Locate platelets.
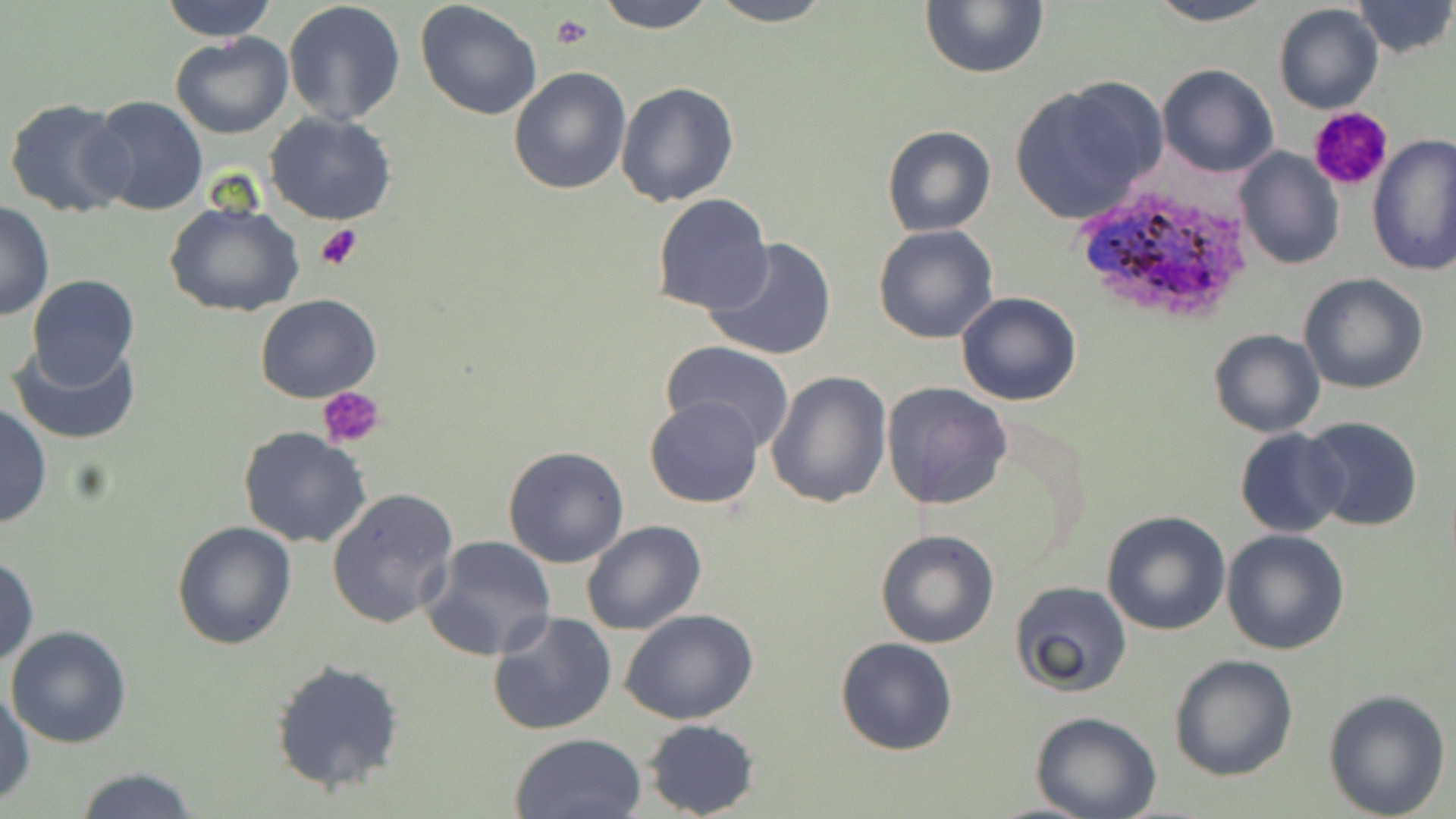
Approximate bounding boxes as [x1, y1, x2, y2] in pixels.
Platelets: [550, 14, 592, 50], [1309, 106, 1394, 191], [315, 222, 365, 271], [319, 386, 386, 450].

{
  "plasmodium_ovale_infected_red_blood_cell_locations": "approximate bounding boxes as [x1, y1, x2, y2] in pixels: [1068, 184, 1258, 326]",
  "slide_level_diagnosis": "Plasmodium ovale",
  "preparation": "thin blood film",
  "image_size": "1456×819 pixels",
  "field_of_view": "one of a larger specimen",
  "modality": "light microscopy",
  "stain": "May-Grünwald-Giemsa",
  "uninfected_red_blood_cell_locations": "approximate bounding boxes as [x1, y1, x2, y2] in pixels: [161, 0, 276, 42], [282, 0, 406, 126], [596, 0, 715, 33], [706, 0, 835, 27], [920, 0, 1049, 78], [1141, 0, 1282, 27], [1349, 0, 1455, 59], [415, 1, 542, 120], [1272, 3, 1384, 116], [169, 31, 293, 139], [1156, 63, 1278, 178], [508, 66, 632, 195], [1010, 78, 1166, 225], [616, 81, 740, 208], [88, 94, 209, 215], [4, 97, 132, 220], [263, 110, 398, 226], [881, 124, 997, 237], [1368, 134, 1456, 275], [1232, 145, 1343, 270], [651, 192, 775, 315], [1, 198, 53, 322], [164, 200, 304, 317], [873, 225, 1000, 344], [704, 237, 837, 362], [1297, 272, 1429, 395], [25, 274, 139, 390], [255, 292, 380, 403], [954, 292, 1082, 407], [1207, 328, 1325, 438], [8, 338, 142, 445], [660, 342, 795, 451], [766, 371, 893, 508], [880, 381, 1013, 508], [644, 394, 765, 509], [0, 405, 51, 529], [1301, 418, 1424, 533], [238, 427, 371, 549], [1234, 428, 1347, 536], [503, 445, 631, 568], [327, 487, 459, 631], [1100, 509, 1232, 635], [171, 520, 296, 650], [581, 520, 707, 637], [876, 528, 999, 649], [1220, 528, 1350, 655], [421, 535, 558, 659], [0, 555, 37, 669], [1008, 581, 1132, 699], [619, 607, 760, 726], [488, 611, 617, 736], [5, 625, 133, 749], [834, 636, 960, 755], [1168, 653, 1299, 780], [271, 657, 407, 794], [0, 687, 35, 808], [1323, 687, 1451, 818], [1031, 712, 1163, 819], [641, 718, 760, 817], [508, 732, 647, 819], [70, 766, 201, 819]",
  "magnification": "1000x"
}